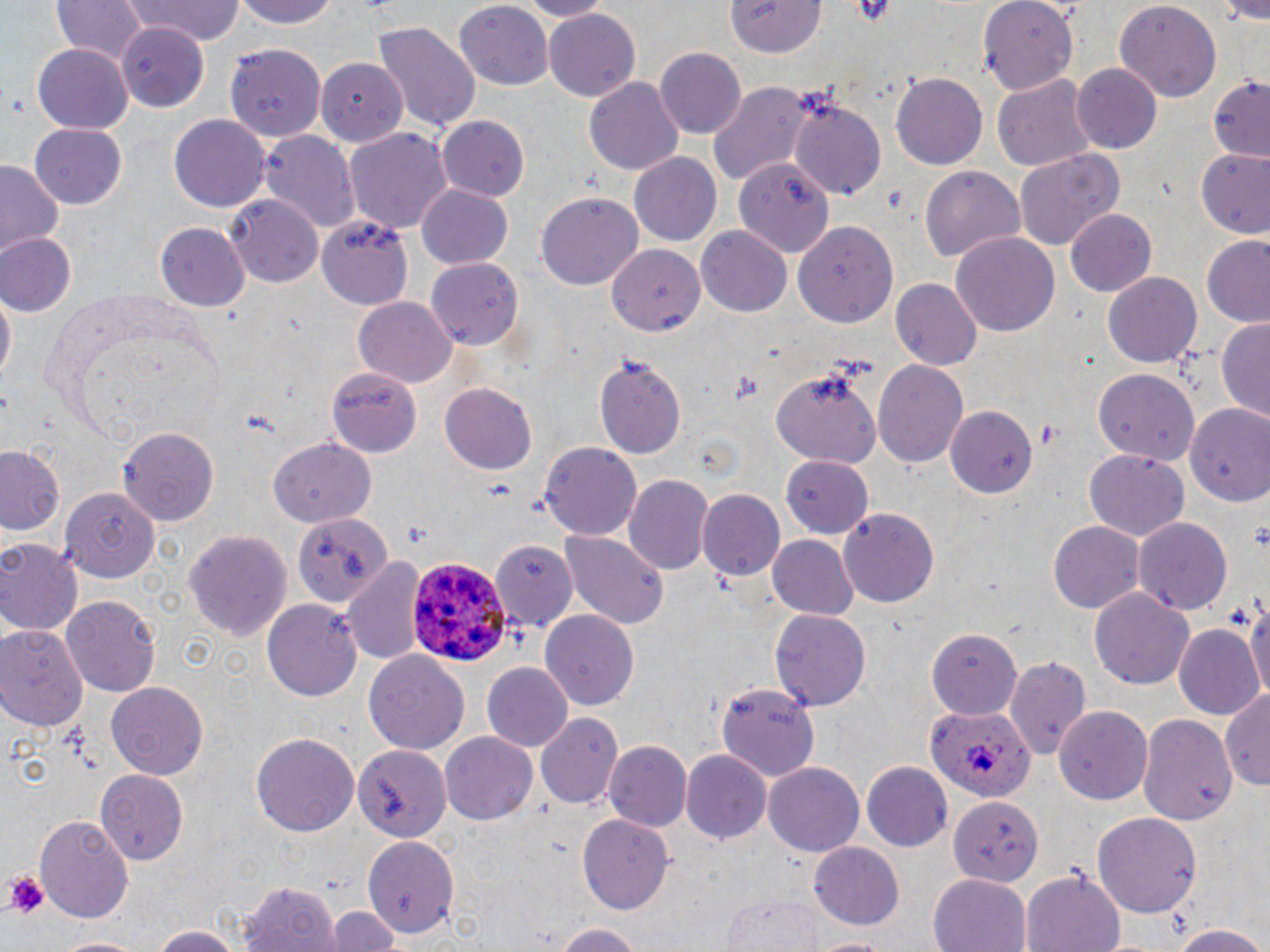 Approximate bounding boxes as (x1,y1)-(x2,y2) corner pairs in pixels. Platelet locations: (4,873)-(47,918). Plasmodium ovale-infected red blood cell locations: (406,553)-(509,665), (925,705)-(1034,801). Uninfected red blood cell locations: (47,0)-(152,66), (124,0)-(247,44), (233,0)-(339,31), (516,0)-(611,20), (727,0)-(828,58), (976,0)-(1077,94), (1112,2)-(1222,105), (454,4)-(555,88), (543,9)-(640,100), (372,21)-(481,135), (116,22)-(212,110), (225,44)-(324,140), (33,45)-(134,133), (656,48)-(746,139), (314,56)-(407,145), (1072,63)-(1163,154), (891,72)-(987,168), (992,73)-(1095,174), (582,75)-(684,177), (1206,76)-(1270,160), (708,81)-(813,185), (785,91)-(886,198), (168,113)-(271,212), (437,114)-(529,202), (29,122)-(127,208), (345,128)-(453,235), (260,130)-(360,235), (1015,148)-(1126,250), (1193,149)-(1270,239), (629,153)-(722,248), (736,157)-(838,263), (0,161)-(66,262), (919,165)-(1026,265), (417,184)-(513,268), (536,192)-(644,290), (227,196)-(323,286), (1063,208)-(1157,297), (318,214)-(416,308), (794,221)-(899,328), (155,224)-(248,311), (696,226)-(792,316), (951,232)-(1061,337), (1,233)-(77,315), (1200,237)-(1270,327), (607,243)-(706,335), (426,259)-(523,348), (1103,272)-(1201,367), (892,277)-(982,371), (0,286)-(15,391), (353,296)-(457,387), (1215,316)-(1270,424), (594,352)-(686,458), (874,356)-(969,470), (773,363)-(884,469), (326,365)-(422,456), (1092,367)-(1200,465), (439,384)-(536,474), (1186,403)-(1270,506), (945,408)-(1035,499), (118,427)-(219,525), (270,440)-(375,529), (0,444)-(65,538), (538,444)-(641,538), (1082,450)-(1188,544), (782,454)-(874,539), (625,474)-(713,575), (59,487)-(157,579), (697,487)-(784,582), (837,508)-(940,609), (295,511)-(391,609), (1134,517)-(1232,617), (1048,521)-(1146,611), (183,527)-(291,640), (561,530)-(666,631), (768,535)-(860,621), (0,537)-(82,636), (489,540)-(577,630), (346,556)-(427,667), (1090,586)-(1195,689), (1243,589)-(1270,705), (62,594)-(159,698), (264,598)-(363,704), (542,610)-(640,711), (770,610)-(871,712), (0,623)-(86,730), (1173,623)-(1264,721), (926,628)-(1022,719), (363,649)-(470,756), (1006,657)-(1091,760), (482,663)-(573,753), (105,681)-(209,780), (715,683)-(821,780), (1222,687)-(1270,794), (1054,706)-(1152,808), (536,712)-(622,808), (1138,715)-(1236,825), (251,732)-(359,836), (440,734)-(537,823), (603,741)-(689,832), (356,744)-(452,841), (680,747)-(771,843), (765,763)-(863,855), (862,763)-(951,850), (97,770)-(188,865), (947,794)-(1040,885), (1094,810)-(1201,920), (36,814)-(135,924), (578,814)-(674,912), (360,835)-(461,939), (807,843)-(905,931), (1021,867)-(1126,952), (927,872)-(1032,952), (241,881)-(342,952), (722,895)-(825,951), (323,907)-(404,952), (543,921)-(652,951), (149,923)-(248,952), (1167,923)-(1270,951), (55,934)-(137,952), (808,935)-(900,952). Slide-level diagnosis: Plasmodium ovale. Image is 1270×952 pixels. Thin blood film. Optical microscopy. Captured at 1000x magnification. One field of a larger specimen. May-Grünwald-Giemsa stain.